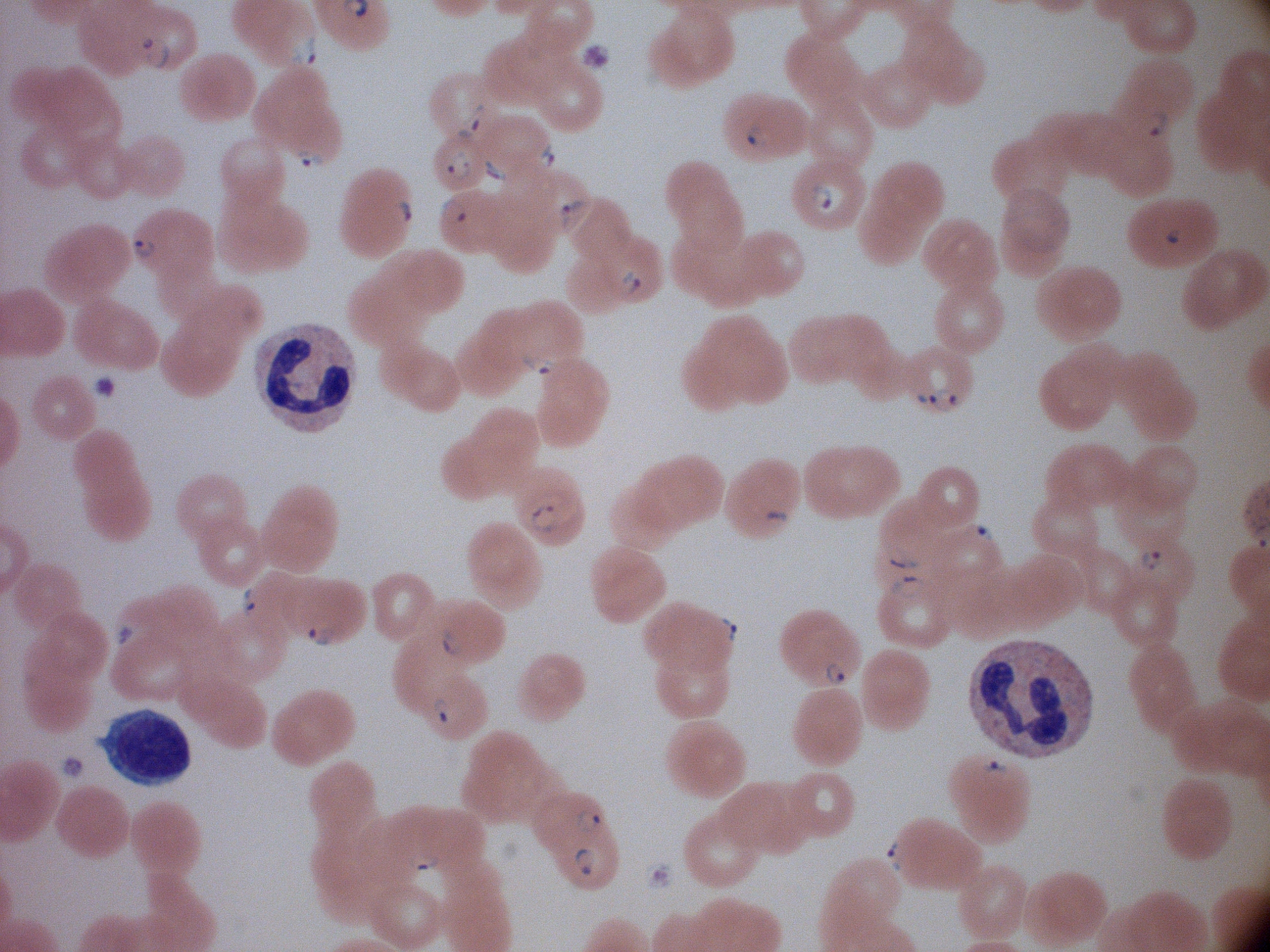

field_of_view: single
image_size: 1270×952 pixels
preparation: thin blood film
stain: Giemsa
ring_form_locations: 'approximate bounding boxes as named x1/y1/x2/y2 corners in pixels, from the source annotation, which is not necessarily exhaustive: (x1=138, y1=34, x2=174, y2=70), (x1=285, y1=34, x2=320, y2=66), (x1=457, y1=101, x2=487, y2=143), (x1=1141, y1=102, x2=1172, y2=141), (x1=742, y1=120, x2=774, y2=154), (x1=537, y1=141, x2=560, y2=171), (x1=291, y1=145, x2=327, y2=172), (x1=445, y1=148, x2=472, y2=185), (x1=480, y1=157, x2=510, y2=185), (x1=557, y1=193, x2=590, y2=233), (x1=390, y1=195, x2=413, y2=230), (x1=440, y1=196, x2=470, y2=225), (x1=127, y1=231, x2=162, y2=262), (x1=617, y1=267, x2=644, y2=300), (x1=521, y1=352, x2=560, y2=376), (x1=910, y1=387, x2=961, y2=414), (x1=529, y1=501, x2=561, y2=536), (x1=761, y1=507, x2=789, y2=532), (x1=965, y1=520, x2=998, y2=545), (x1=881, y1=541, x2=918, y2=571), (x1=1136, y1=546, x2=1164, y2=575), (x1=890, y1=571, x2=928, y2=599), (x1=239, y1=586, x2=263, y2=621), (x1=715, y1=615, x2=745, y2=649), (x1=303, y1=623, x2=338, y2=648), (x1=438, y1=625, x2=465, y2=658), (x1=821, y1=661, x2=848, y2=688), (x1=432, y1=692, x2=460, y2=725), (x1=977, y1=752, x2=1009, y2=780), (x1=576, y1=806, x2=604, y2=837), (x1=883, y1=839, x2=908, y2=871), (x1=570, y1=847, x2=599, y2=878), (x1=407, y1=849, x2=440, y2=871)'
species: Plasmodium falciparum
microscope: Leica DM2000 with built-in camera
magnification: 100x